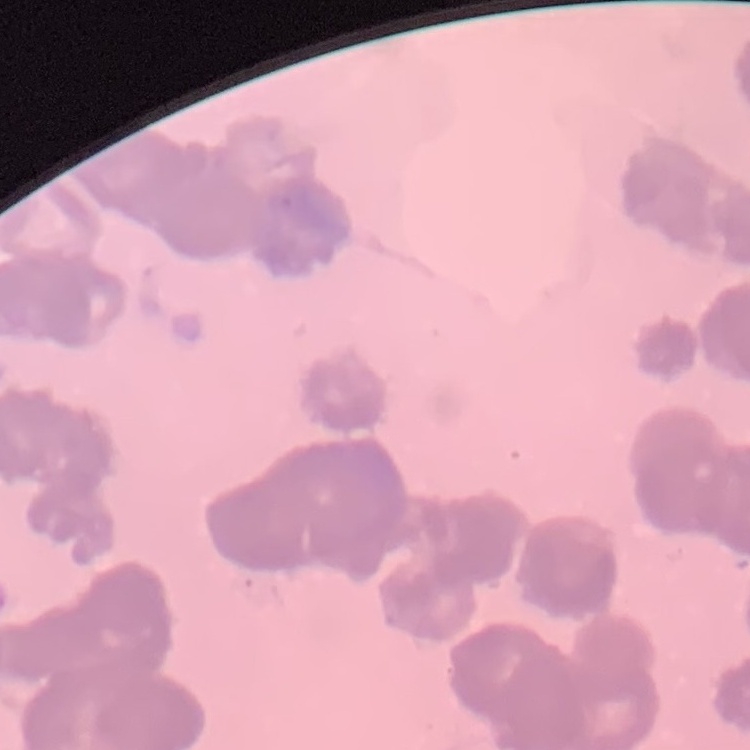

Summary:
  - Erythrocyte morphology: rouleaux formation
  - Preparation: thin blood smear
  - Image type: one tile cut from a larger photomicrograph
  - Stain: Field's or Giemsa